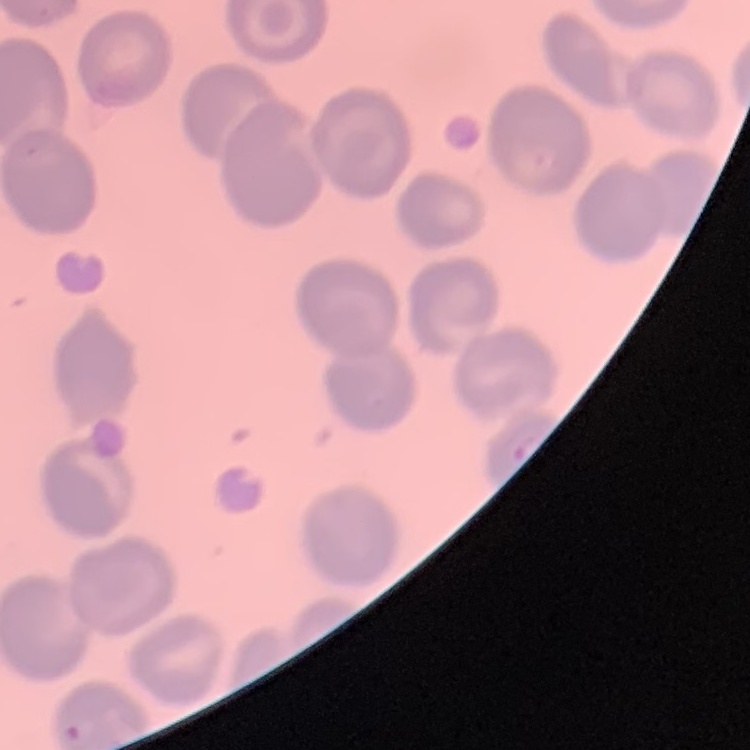
The red blood cells show no rouleaux formation. Stained with either Field's or Giemsa. Square crop of a larger photomicrograph. Thin blood film.